Point out each Plasmodium parasite.
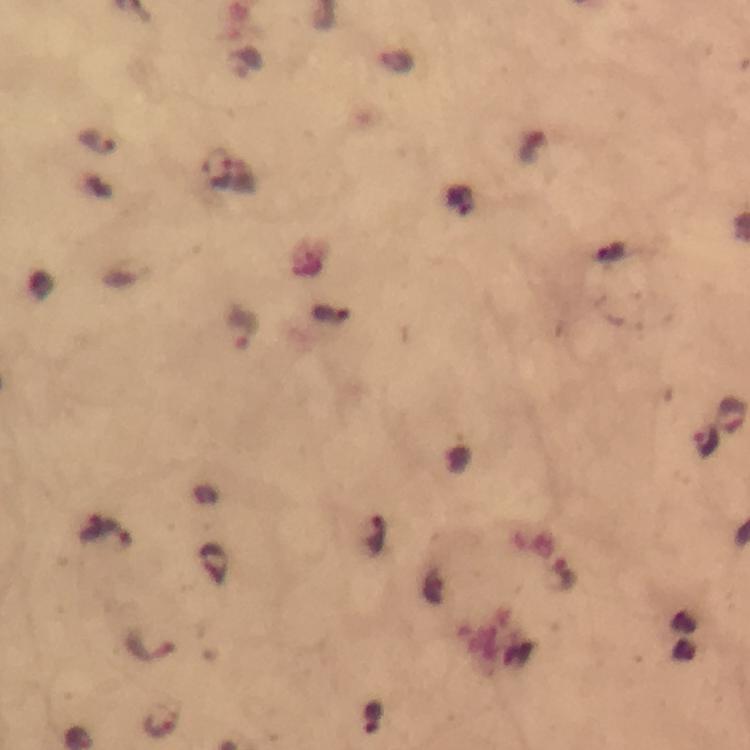
Approximate centers as (x, y) in pixels.
Plasmodium parasites: (98, 143), (217, 167), (330, 313), (244, 330), (732, 414), (708, 441), (104, 533), (376, 537), (560, 576), (150, 643), (374, 719), (162, 721).

stain = Giemsa
image size = 750×750 pixels
preparation = thick smear
capture = smartphone camera through the microscope
magnification = 100x
context = from a malaria diagnostic workup
cropped from = a single field of view
immersion oil = applied